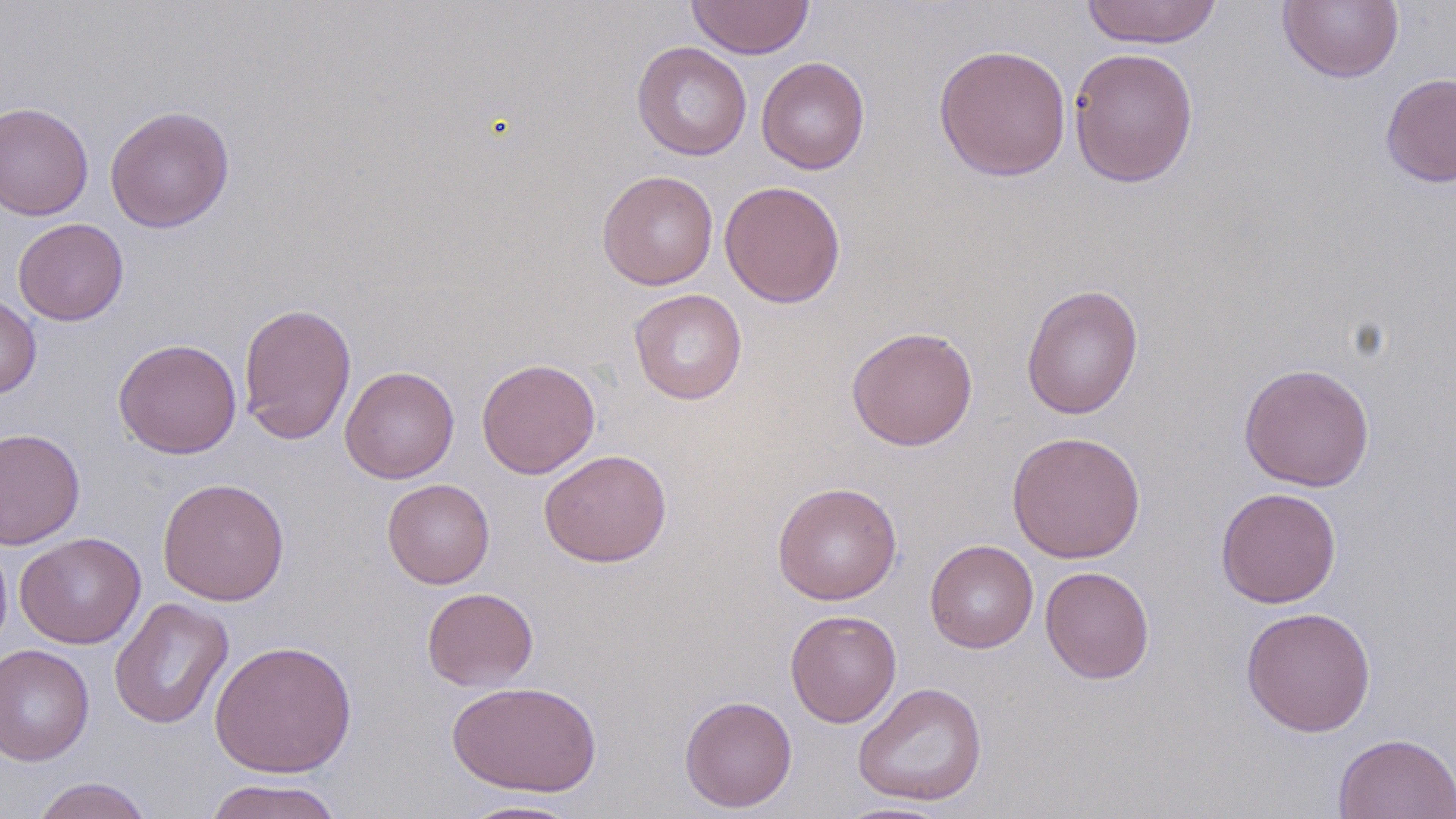

Approximate bounding boxes as (x1, y1, x2, y2) in pixels. Uninfected red blood cell locations: (1080, 0, 1222, 48), (1277, 0, 1405, 84), (686, 1, 814, 59), (632, 41, 752, 160), (933, 43, 1072, 182), (1068, 47, 1199, 187), (756, 57, 870, 174), (1380, 72, 1456, 188), (0, 100, 94, 221), (104, 105, 235, 233), (596, 169, 719, 290), (720, 180, 846, 308), (13, 218, 128, 325), (1021, 283, 1144, 420), (629, 288, 747, 405), (0, 293, 41, 399), (237, 302, 357, 445), (845, 326, 979, 451), (113, 339, 242, 459), (476, 358, 601, 479), (1238, 362, 1375, 492), (340, 366, 460, 483), (0, 427, 85, 550), (1006, 430, 1146, 564), (539, 448, 672, 567), (157, 477, 290, 606), (382, 478, 495, 588), (772, 481, 902, 605), (1215, 487, 1342, 608), (14, 532, 146, 649), (0, 535, 12, 656), (924, 539, 1038, 653), (1040, 565, 1155, 684), (422, 587, 539, 691), (109, 597, 235, 730), (1240, 605, 1377, 737), (785, 609, 901, 727), (209, 639, 358, 777), (0, 643, 95, 765), (445, 680, 602, 797), (852, 682, 987, 806), (679, 695, 797, 812), (1333, 732, 1456, 819), (30, 777, 155, 819), (202, 777, 345, 819), (453, 798, 587, 818), (832, 800, 959, 818). Slide-level diagnosis: negative for blood parasites. Captured at 1000x magnification. Image is 1456×819 pixels. May-Grünwald-Giemsa stain. One field of a larger specimen. Light microscopy. Thin blood smear.